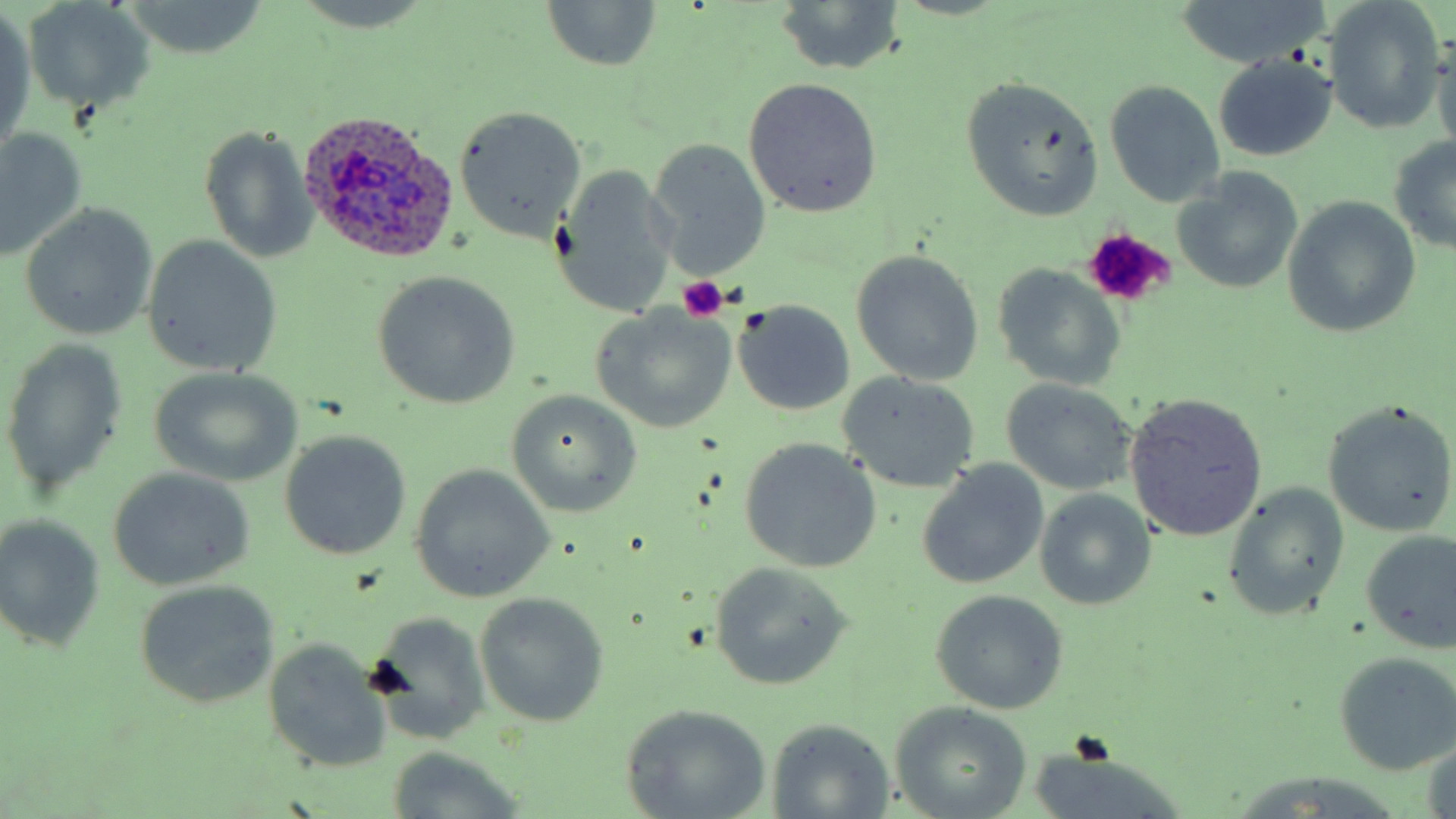

Approximate bounding boxes as (x1, y1, x2, y2) in pixels. Uninfected red blood cell locations: (19, 0, 156, 118), (540, 0, 663, 74), (1177, 0, 1326, 69), (1322, 0, 1446, 137), (770, 2, 904, 74), (1, 10, 36, 160), (1433, 35, 1456, 153), (1212, 55, 1337, 162), (959, 76, 1105, 221), (742, 78, 884, 218), (1104, 81, 1225, 207), (452, 106, 587, 242), (0, 128, 86, 263), (200, 128, 317, 262), (1388, 134, 1456, 254), (647, 139, 772, 279), (551, 162, 680, 319), (1172, 169, 1305, 296), (1283, 197, 1422, 338), (19, 202, 158, 341), (142, 235, 283, 379), (849, 250, 985, 386), (992, 264, 1125, 390), (371, 272, 521, 409), (733, 301, 855, 417), (589, 305, 738, 433), (2, 340, 128, 496), (147, 367, 302, 486), (838, 373, 981, 494), (999, 378, 1139, 495), (506, 390, 642, 517), (1124, 393, 1268, 543), (1322, 401, 1455, 536), (279, 429, 412, 561), (739, 438, 881, 573), (915, 461, 1050, 589), (409, 466, 554, 602), (108, 468, 256, 590), (1222, 485, 1350, 622), (1034, 489, 1156, 611), (1, 516, 105, 653), (1359, 528, 1456, 654), (707, 561, 854, 690), (134, 581, 281, 710), (928, 590, 1069, 714), (473, 592, 610, 729), (366, 611, 493, 744), (263, 637, 392, 773), (1332, 651, 1456, 775), (890, 702, 1032, 819), (620, 704, 774, 819), (766, 718, 896, 817), (1420, 737, 1456, 819), (1025, 747, 1190, 819), (383, 748, 526, 816), (1221, 774, 1414, 819). Platelet locations: (1083, 230, 1176, 304), (678, 275, 729, 322). Plasmodium ovale-infected red blood cell locations: (293, 109, 462, 268). Slide-level diagnosis: Plasmodium ovale. Thin blood film. 1000x magnification. May-Grünwald-Giemsa-stained preparation. One field of a larger specimen. Image is 1456×819 pixels. Optical microscopy.